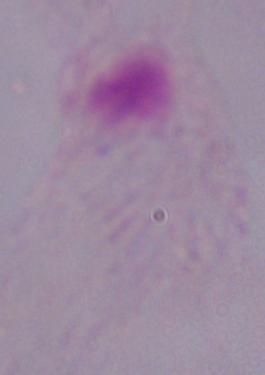

identification = trichomonad
modality = photomicrograph
magnification = 1000x